Locate every Plasmodium parasite.
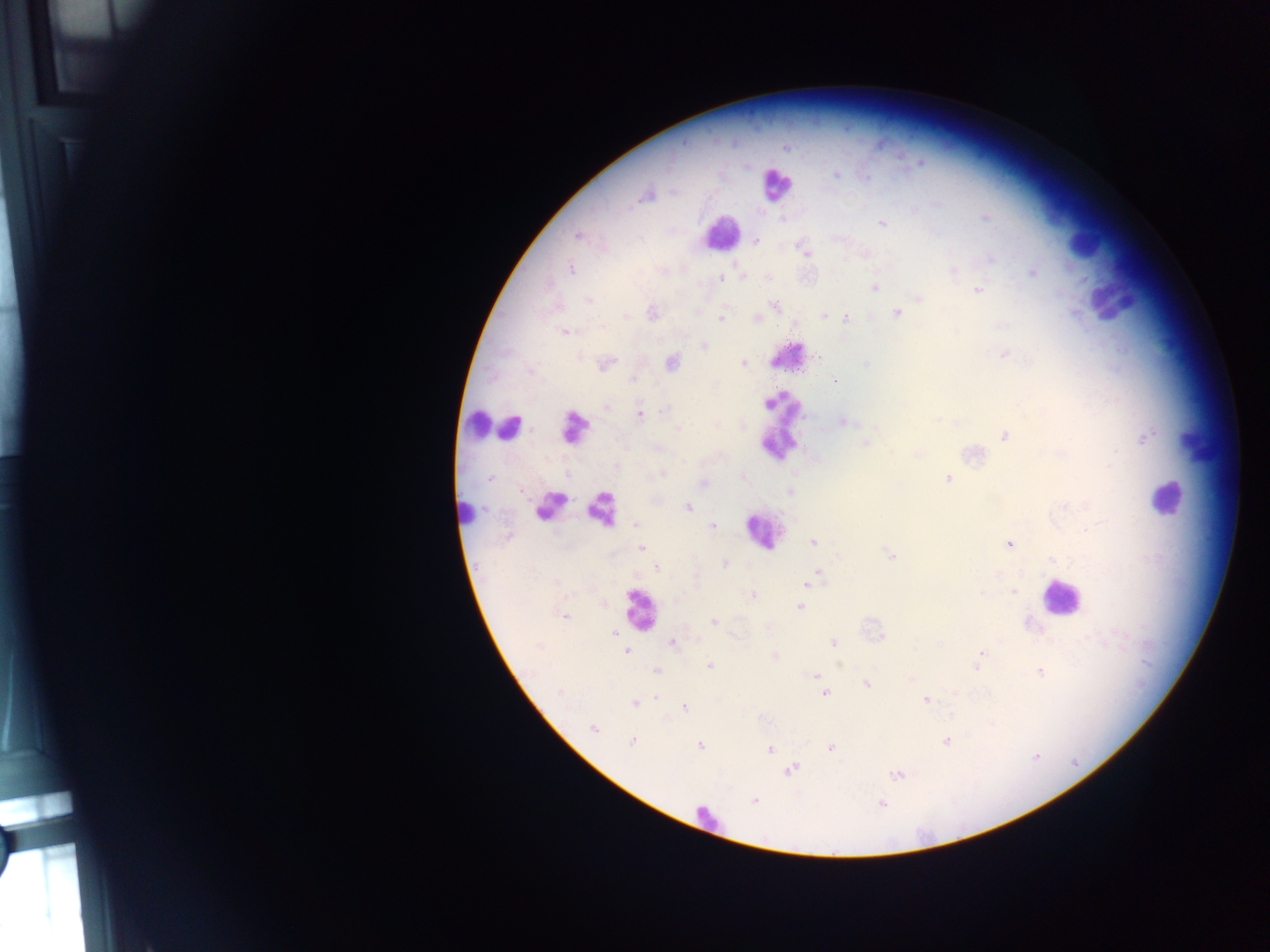
Approximate centers as (x, y) in pixels.
Plasmodium parasites: (836, 174), (646, 196), (985, 217), (782, 219), (881, 223), (577, 237), (755, 241), (807, 253), (571, 269), (954, 270), (1033, 273), (744, 276), (768, 277), (720, 278), (875, 288), (978, 290), (918, 298), (588, 300), (775, 305), (653, 312), (897, 313), (626, 316), (823, 316), (721, 318), (756, 318), (846, 318), (602, 326), (565, 332), (704, 346), (1005, 354), (671, 362), (606, 363), (743, 364), (530, 371), (632, 379), (835, 381), (606, 405), (665, 409), (640, 416), (843, 422), (677, 428), (1004, 436), (1144, 438), (865, 443), (1062, 453), (615, 465), (1109, 465), (663, 473), (742, 477), (491, 478), (948, 479), (702, 484), (790, 491), (687, 507), (636, 524), (713, 526), (813, 542), (1009, 543), (641, 548), (891, 556), (1052, 559), (724, 564), (657, 568), (819, 573), (697, 579), (808, 583), (1014, 592), (752, 595), (800, 606), (566, 617), (714, 621), (614, 634), (882, 637), (672, 643), (833, 643), (539, 647), (625, 651), (981, 653), (775, 656), (710, 666), (977, 667), (655, 671), (1039, 671), (817, 675), (866, 684), (560, 693), (824, 694), (657, 698), (925, 700), (635, 703), (684, 707), (593, 729), (632, 741), (946, 741), (700, 745), (830, 747), (770, 749), (791, 770), (896, 775), (754, 800), (882, 804).

{
  "image_size": "1270×952 pixels",
  "leukocyte_locations": "approximate centers as (x, y) in pixels: (775, 185), (721, 233), (1080, 245), (1113, 294), (785, 360), (471, 422), (781, 422), (510, 427), (575, 427), (1196, 442), (1165, 498), (549, 505), (601, 510), (469, 512), (762, 531), (1059, 598), (639, 608), (703, 816)",
  "country": "Ghana",
  "preparation": "thick blood smear",
  "field_of_view": "single",
  "capture": "mobile-phone photograph through a microscope"
}